Locate the cells, classifying each as a parasitized red blood cell, an uninfected red blood cell, or a white blood cell.
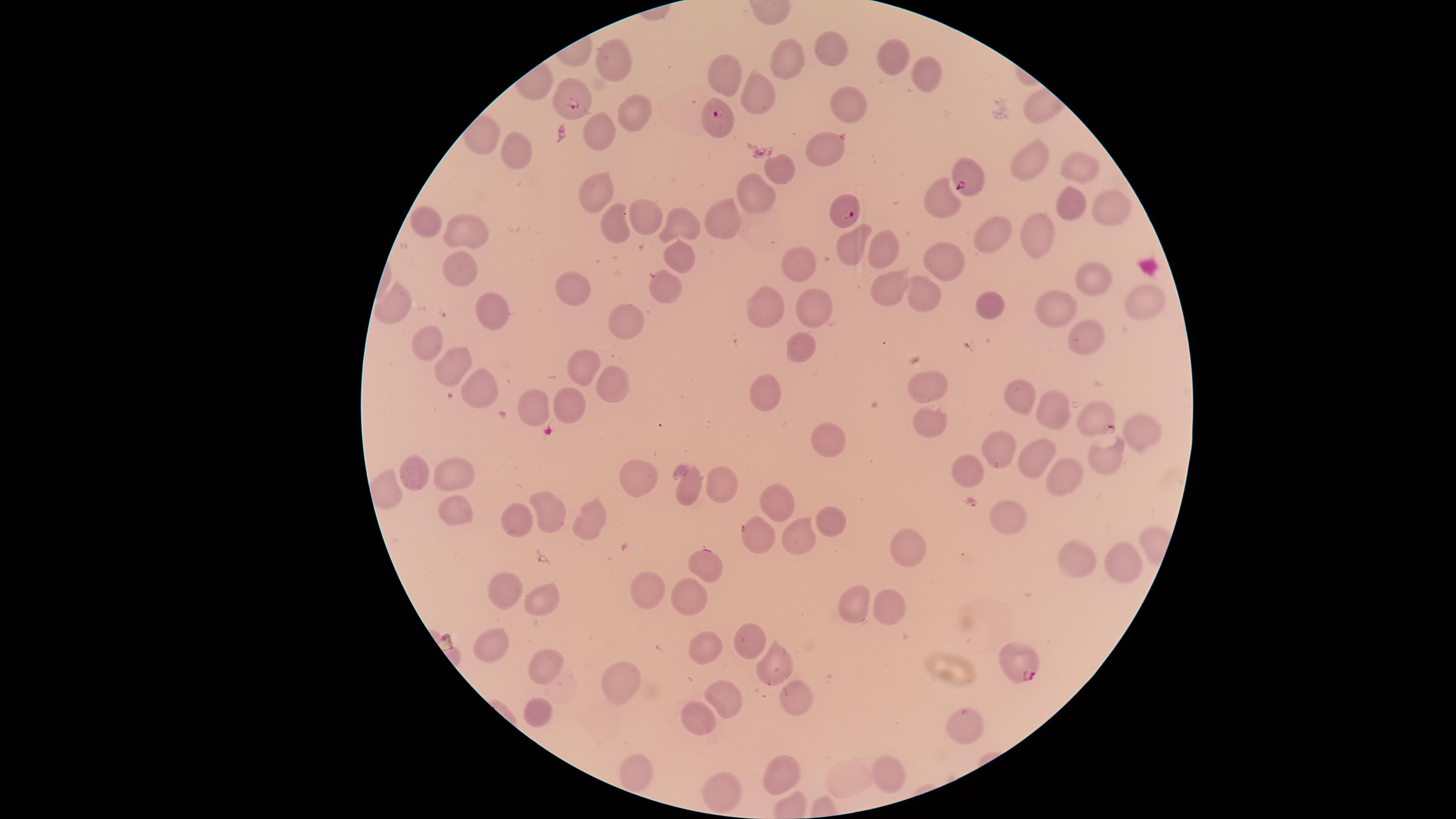
Approximate marker points, in pixels from the top-left corner.
Parasitized red blood cells: (x=570, y=99), (x=717, y=117), (x=965, y=184), (x=842, y=208), (x=1025, y=662).
Uninfected red blood cells: (x=832, y=46), (x=615, y=56), (x=787, y=62), (x=899, y=62), (x=728, y=70), (x=926, y=72), (x=759, y=92), (x=855, y=106), (x=633, y=112), (x=600, y=132), (x=826, y=149), (x=509, y=150), (x=1079, y=162), (x=1030, y=165), (x=775, y=168), (x=601, y=190), (x=756, y=192), (x=941, y=197), (x=1072, y=201), (x=1104, y=206), (x=641, y=213), (x=727, y=219), (x=611, y=222), (x=676, y=223), (x=429, y=225), (x=995, y=231), (x=1036, y=231), (x=473, y=234), (x=855, y=240), (x=889, y=249), (x=678, y=255), (x=944, y=257), (x=458, y=265), (x=799, y=265), (x=1090, y=277), (x=888, y=283), (x=668, y=286), (x=923, y=293), (x=1138, y=293), (x=578, y=295), (x=395, y=302), (x=1054, y=306), (x=767, y=308), (x=994, y=308), (x=491, y=311), (x=815, y=311), (x=627, y=320), (x=1086, y=334), (x=799, y=348), (x=428, y=351), (x=585, y=364), (x=454, y=372), (x=482, y=388), (x=933, y=389), (x=610, y=394), (x=1017, y=394), (x=766, y=396), (x=566, y=401), (x=535, y=403), (x=1050, y=409), (x=1090, y=415), (x=927, y=421), (x=1143, y=429), (x=828, y=440), (x=996, y=448), (x=1043, y=458), (x=1105, y=462), (x=453, y=470), (x=641, y=474), (x=423, y=475), (x=1066, y=479), (x=967, y=482), (x=691, y=484), (x=724, y=485), (x=774, y=499), (x=447, y=508), (x=1010, y=508), (x=549, y=514), (x=828, y=515), (x=520, y=520), (x=591, y=522), (x=751, y=538), (x=796, y=539), (x=908, y=547), (x=1078, y=561), (x=704, y=567), (x=1119, y=568), (x=645, y=592), (x=688, y=592), (x=501, y=593), (x=541, y=599), (x=886, y=604), (x=854, y=607), (x=752, y=638), (x=489, y=640), (x=709, y=643), (x=542, y=658), (x=774, y=665), (x=623, y=682), (x=730, y=696), (x=794, y=704), (x=536, y=714), (x=699, y=716), (x=963, y=728), (x=634, y=766), (x=782, y=766), (x=893, y=770), (x=716, y=792).
No white blood cells identified.

field of view = single
preparation = thin blood film
capture = smartphone photograph through the microscope eyepiece
image size = 1456×819 pixels
visible region = circular
stain = Giemsa
species = Plasmodium falciparum